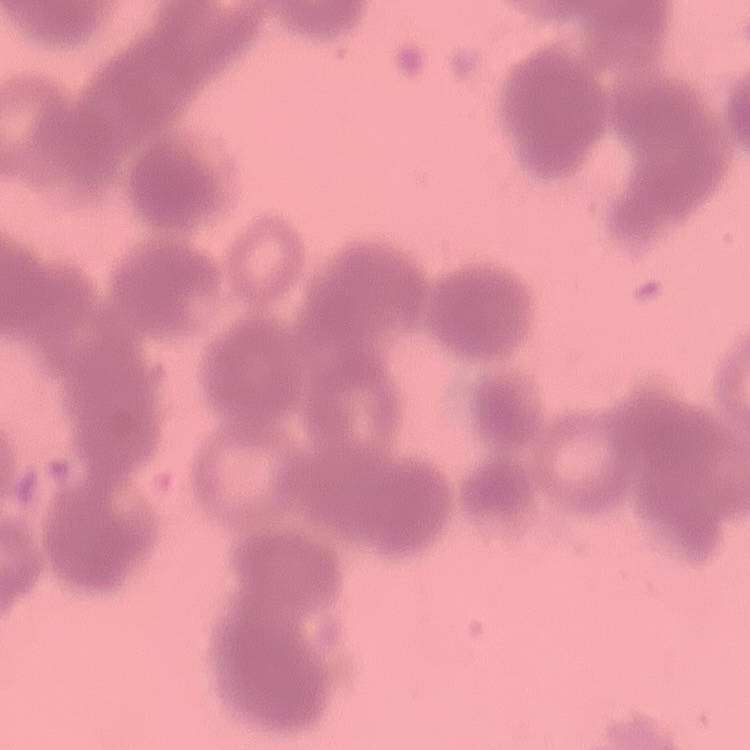

erythrocyte morphology = rouleaux formation
image type = one tile cut from a larger photomicrograph
preparation = thin blood smear
stain = Field's or Giemsa